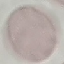

result = no malaria parasites detected
preparation = thin smear
image type = cell patch, automatically extracted from a larger field of view and resized to 64 × 64 pixels
capture = smartphone through the microscope eyepiece
stain = Giemsa